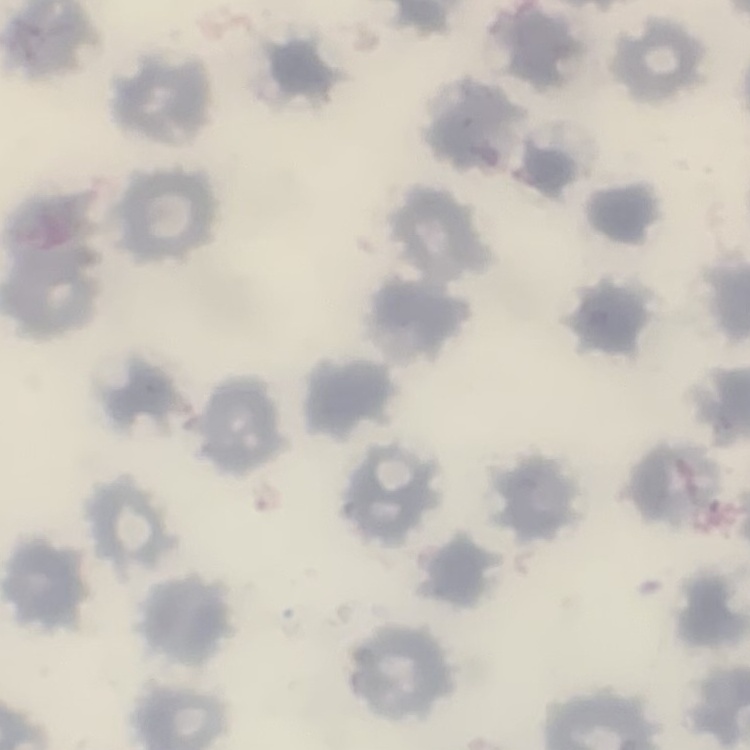 The red blood cells exhibit no rouleaux formation. Field's or Giemsa stain. One tile cut from a larger photomicrograph. Thin peripheral smear.